Give the preparation type.
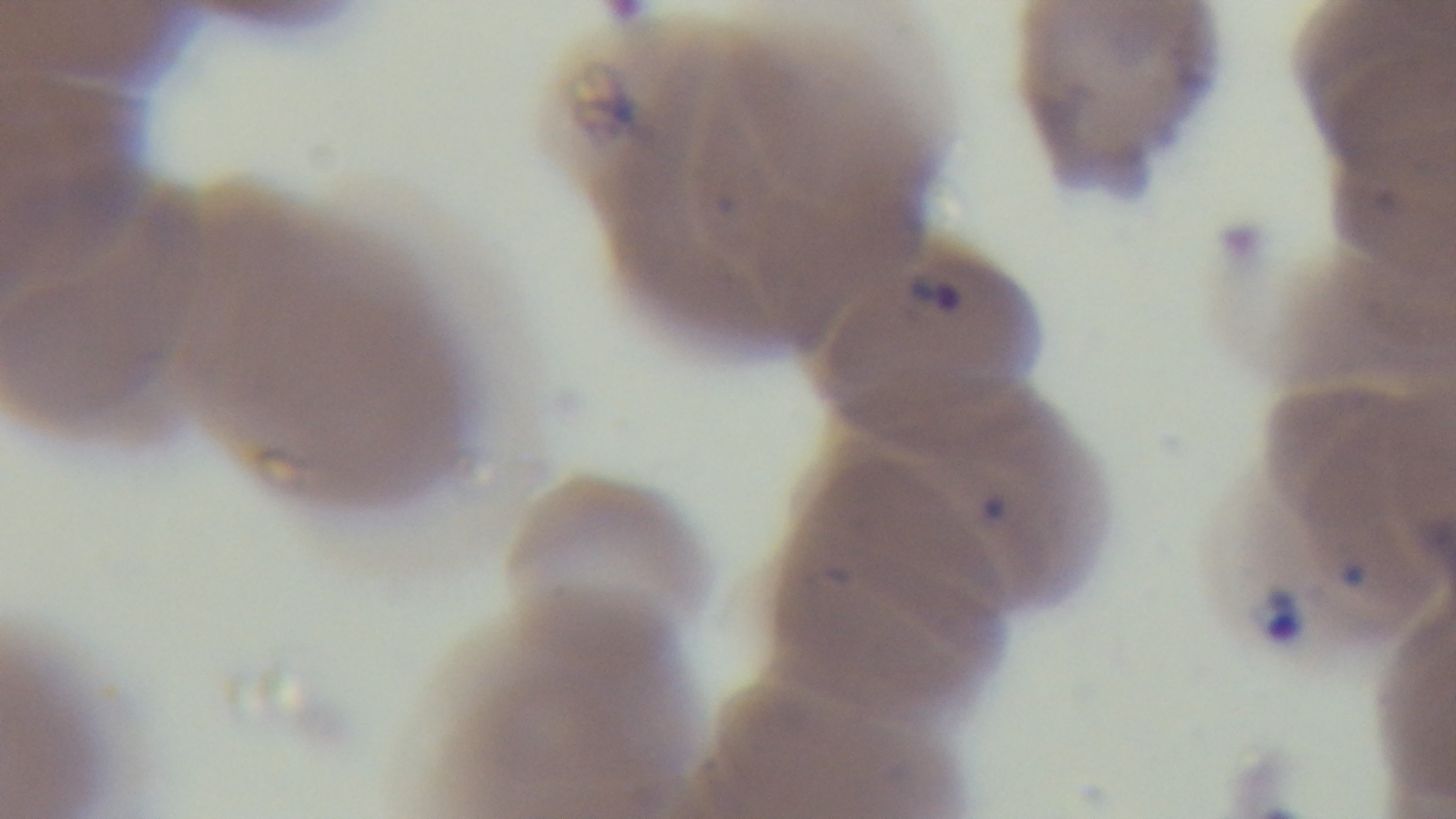
A thin smear.

Giemsa-stained. Oil-immersion objective, 100x. Malaria status: infected. Single field of view. Light microscopy. Captured with a mounted 4K digital camera.